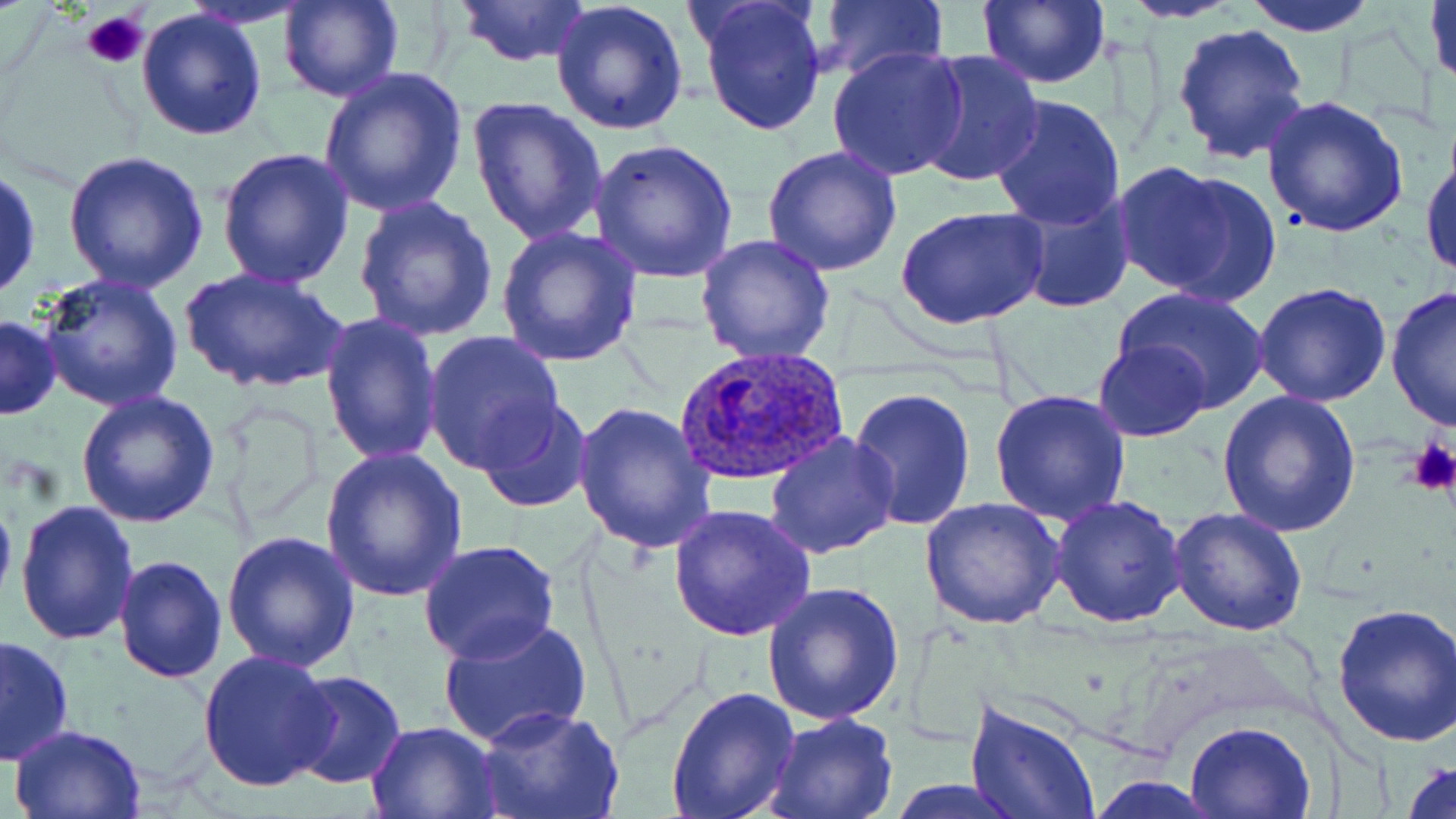

Approximate bounding boxes as [x1, y1, x2, y2] in pixels. Uninfected red blood cell locations: [277, 0, 403, 103], [454, 0, 591, 68], [694, 0, 828, 137], [976, 0, 1110, 89], [1240, 0, 1383, 36], [1426, 0, 1456, 94], [550, 1, 691, 137], [817, 1, 948, 82], [1119, 1, 1246, 23], [137, 6, 269, 141], [1171, 22, 1312, 166], [826, 43, 970, 181], [912, 50, 1045, 190], [316, 67, 466, 217], [988, 93, 1130, 230], [1259, 93, 1409, 238], [466, 94, 608, 246], [588, 138, 740, 282], [1421, 144, 1455, 283], [215, 147, 355, 290], [761, 147, 903, 280], [60, 150, 209, 294], [1111, 162, 1271, 303], [0, 164, 42, 303], [1008, 187, 1138, 314], [352, 197, 499, 343], [897, 206, 1049, 332], [494, 224, 643, 367], [694, 233, 836, 365], [178, 266, 348, 396], [35, 271, 186, 413], [1251, 282, 1391, 407], [1113, 286, 1270, 412], [1384, 287, 1455, 433], [319, 311, 444, 467], [1, 314, 62, 419], [423, 329, 567, 474], [1093, 339, 1211, 441], [847, 385, 979, 532], [988, 387, 1134, 526], [76, 389, 222, 527], [1217, 390, 1361, 537], [476, 399, 594, 515], [570, 401, 716, 553], [208, 402, 329, 530], [764, 432, 900, 559], [320, 448, 469, 602], [0, 478, 17, 617], [1049, 495, 1186, 628], [920, 497, 1065, 630], [14, 499, 139, 647], [667, 503, 817, 640], [1167, 508, 1308, 636], [221, 529, 361, 671], [420, 540, 560, 665], [113, 554, 228, 684], [763, 582, 902, 726], [1331, 599, 1456, 747], [437, 615, 592, 749], [0, 633, 75, 766], [198, 652, 339, 794], [286, 670, 406, 789], [666, 684, 800, 819], [967, 697, 1101, 819], [479, 708, 623, 819], [762, 712, 898, 819], [1185, 719, 1316, 818], [365, 720, 500, 817], [10, 723, 149, 817], [1400, 756, 1456, 819], [1087, 777, 1224, 816], [886, 780, 1029, 816]. Plasmodium ovale-infected red blood cell locations: [676, 347, 850, 488]. Platelet locations: [81, 10, 150, 70], [1407, 437, 1456, 495]. Slide-level diagnosis: Plasmodium ovale. Optical microscopy. May-Grünwald-Giemsa stain. 1000x magnification. Image is 1456×819 pixels. Thin blood film. Single field of view.